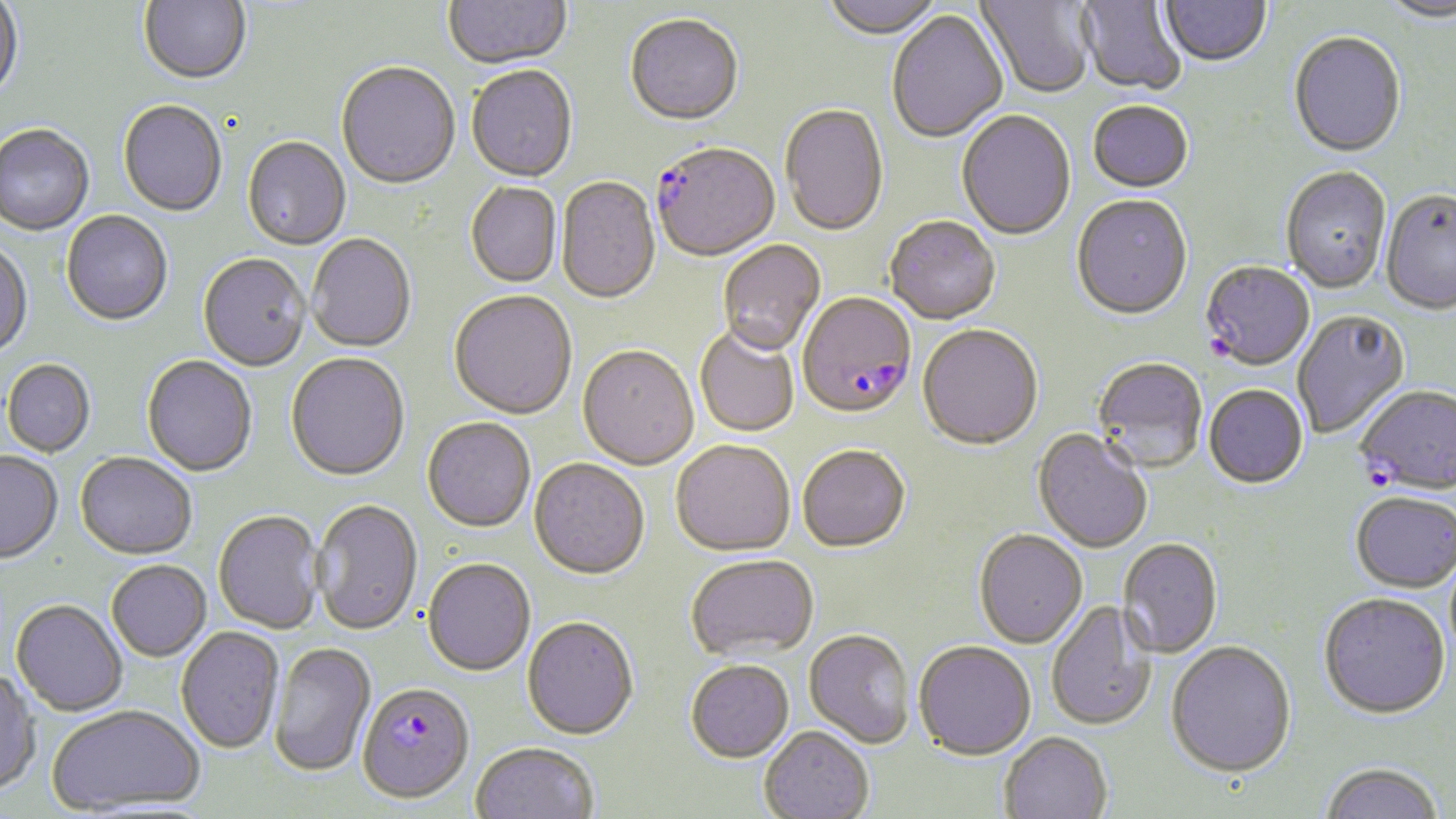
Summary:
  - Coordinate format: approximate bounding boxes as (x1,y1)-(x2,y2) corner pairs in pixels
  - Plasmodium falciparum-infected red blood cell locations: (652,145)-(781,264), (1200,263)-(1315,373), (797,295)-(917,423), (1355,387)-(1456,498), (357,685)-(474,805)
  - Uninfected red blood cell locations: (0,0)-(25,105), (138,0)-(252,87), (444,0)-(572,72), (818,0)-(945,42), (977,0)-(1095,101), (1076,0)-(1188,98), (1379,0)-(1456,26), (1160,1)-(1272,70), (886,11)-(1009,145), (625,16)-(743,129), (1288,34)-(1406,160), (336,64)-(461,192), (466,67)-(578,185), (118,101)-(227,218), (1088,103)-(1193,195), (780,105)-(888,239), (956,111)-(1076,242), (0,126)-(94,237), (242,138)-(351,252), (1281,168)-(1391,295), (556,177)-(661,306), (465,183)-(561,289), (1380,191)-(1456,317), (1071,196)-(1193,323), (61,212)-(173,328), (884,218)-(1001,327), (307,235)-(416,354), (0,241)-(33,360), (717,241)-(826,358), (198,255)-(311,373), (449,292)-(577,422), (1293,311)-(1411,439), (917,326)-(1043,453), (695,327)-(799,438), (577,347)-(699,472), (286,354)-(410,482), (141,356)-(257,477), (1092,359)-(1207,475), (2,360)-(96,457), (1204,386)-(1308,491), (422,419)-(536,534), (1032,430)-(1152,555), (670,442)-(795,559), (797,447)-(911,555), (0,452)-(63,565), (75,454)-(197,561), (529,460)-(650,582), (1350,495)-(1456,595), (311,500)-(423,638), (213,511)-(325,635), (973,531)-(1088,650), (1118,539)-(1223,659), (686,556)-(819,663), (422,560)-(535,677), (106,561)-(211,663), (1318,596)-(1450,722), (10,599)-(128,716), (1046,602)-(1157,732), (521,618)-(639,742), (175,627)-(284,755), (804,630)-(915,750), (270,643)-(376,778), (913,643)-(1036,763), (1165,643)-(1297,781), (685,661)-(794,764), (0,666)-(41,796), (47,705)-(205,814), (759,727)-(874,819), (999,734)-(1112,819), (470,744)-(598,819), (1320,764)-(1443,819)
  - Slide-level diagnosis: Plasmodium falciparum
  - Magnification: 1000x
  - Preparation: thin blood film
  - Modality: optical microscopy
  - Stain: May-Grünwald-Giemsa
  - Field of view: single
  - Image size: 1456×819 pixels